Comment on the morphology of the erythrocytes.
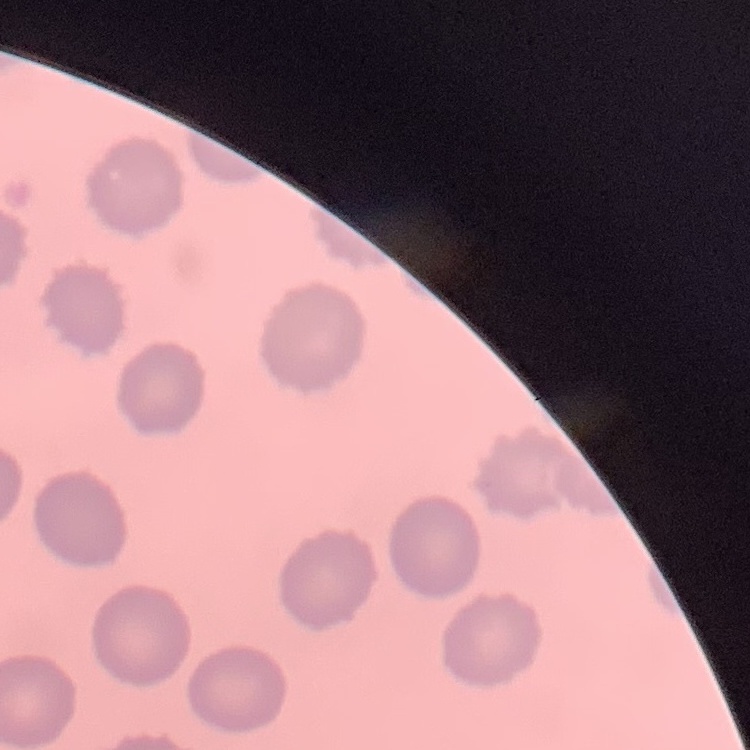
They show no rouleaux formation.

preparation = thin peripheral smear
image type = one tile cut from a larger photomicrograph
stain = Field's or Giemsa